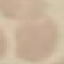
Result: no malaria parasites detected. Acquired by smartphone through the microscope eyepiece. Giemsa-stained preparation. Cell patch, automatically extracted from a larger field of view and resized to 64 × 64 pixels. Thin blood film.